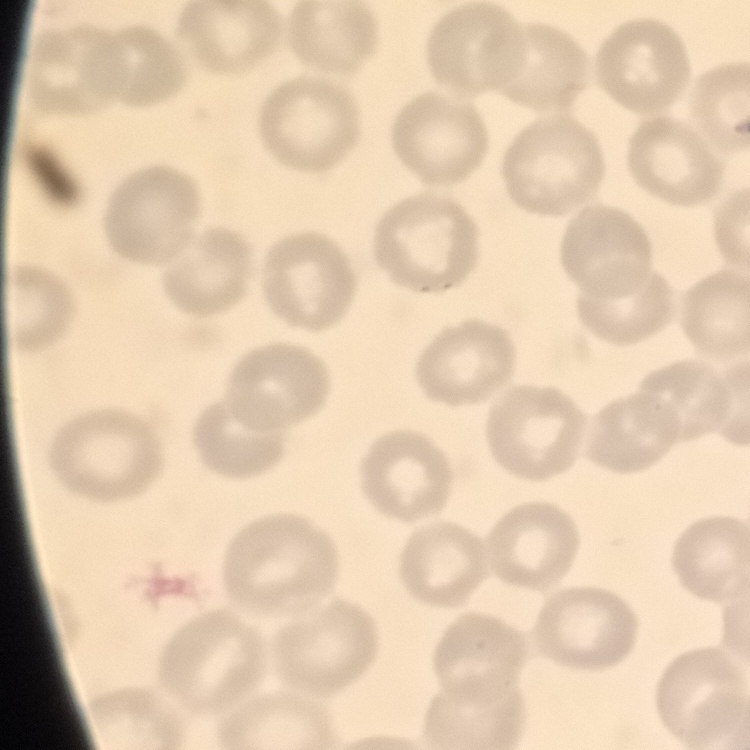

erythrocyte morphology = no rouleaux formation
stain = Field's or Giemsa
preparation = thin blood smear
image type = square crop of a larger photomicrograph